Locate platelets.
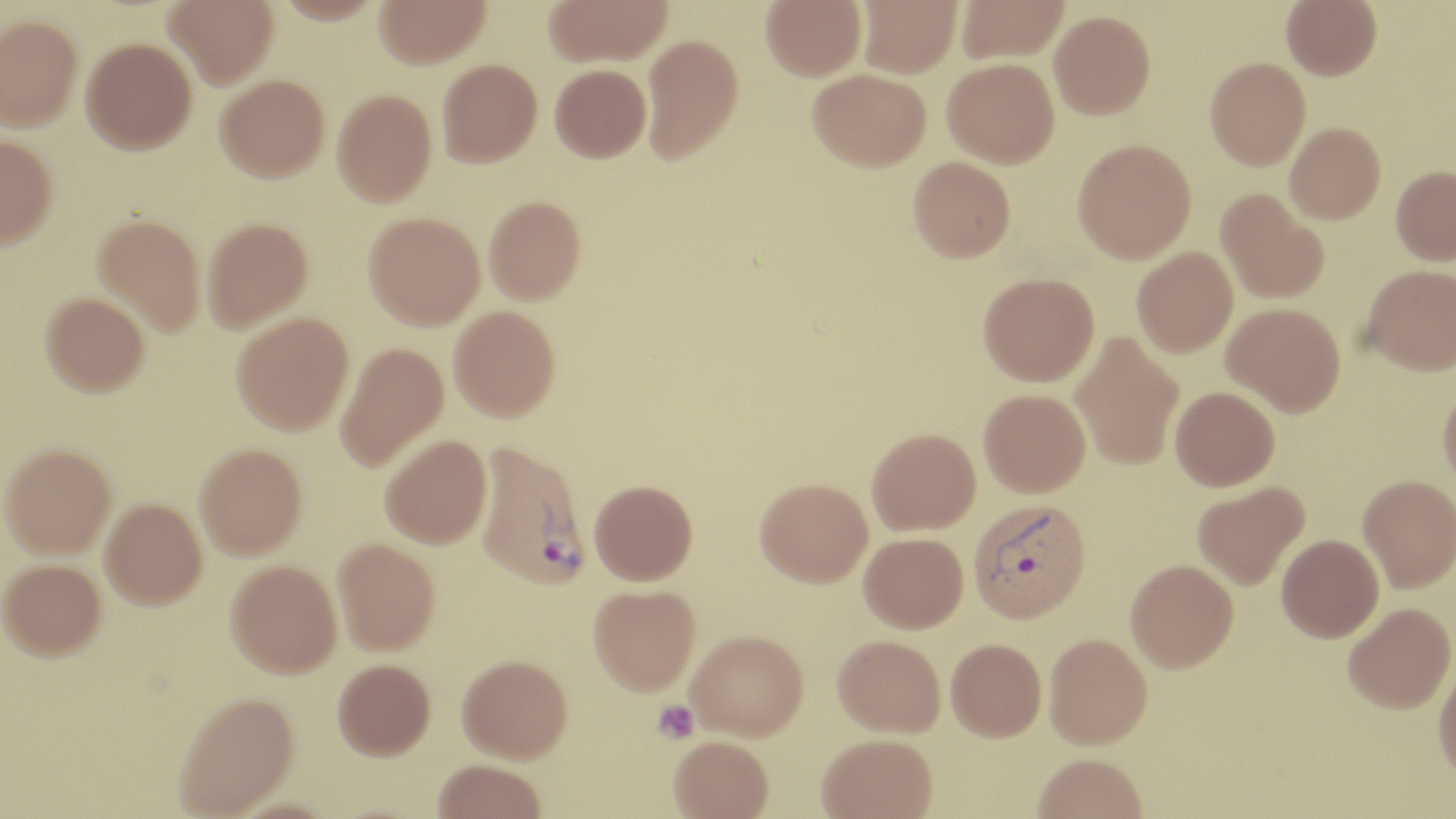

Approximate bounding boxes as (x1,y1)-(x2,y2) corner pairs in pixels.
Platelets: (653,700)-(700,744).

slide_level_diagnosis: Plasmodium vivax
uninfected_red_blood_cell_locations: 'approximate bounding boxes as (x1,y1)-(x2,y2) corner pairs in pixels: (164,0)-(278,88), (374,0)-(490,67), (543,0)-(673,66), (760,0)-(866,81), (857,0)-(962,77), (955,0)-(1070,63), (1281,0)-(1381,80), (1049,10)-(1155,119), (0,14)-(82,130), (641,34)-(744,164), (81,37)-(197,154), (1205,56)-(1310,170), (942,57)-(1060,167), (437,58)-(542,167), (549,64)-(651,162), (807,68)-(931,172), (215,74)-(330,182), (332,89)-(436,207), (1284,122)-(1386,224), (0,135)-(57,251), (1072,138)-(1196,263), (908,156)-(1016,262), (1391,166)-(1456,264), (1215,189)-(1329,304), (483,195)-(586,303), (363,212)-(485,329), (92,213)-(205,335), (202,217)-(313,332), (1132,247)-(1237,357), (1361,264)-(1456,375), (978,271)-(1099,386), (41,292)-(149,396), (1222,303)-(1345,415), (448,305)-(561,421), (231,312)-(353,435), (1069,330)-(1184,471), (334,342)-(449,472), (1437,383)-(1456,493), (1170,386)-(1280,490), (979,388)-(1090,497), (866,428)-(981,535), (379,435)-(492,549), (0,443)-(116,557), (194,443)-(307,559), (1358,474)-(1456,592), (754,477)-(872,587), (589,479)-(698,585), (1192,481)-(1310,590), (100,498)-(207,608), (858,532)-(969,633), (1277,534)-(1384,642), (332,538)-(440,655), (0,559)-(106,659), (225,559)-(342,678), (1125,559)-(1239,672), (588,584)-(700,696), (1342,602)-(1455,714), (686,629)-(808,740), (1044,632)-(1153,750), (833,635)-(946,738), (945,639)-(1046,742), (456,655)-(572,763), (1433,657)-(1456,787), (332,658)-(435,759), (172,690)-(300,818), (817,733)-(938,819), (669,736)-(773,819), (1031,755)-(1147,819), (433,760)-(547,819)'
stain: May-Grünwald-Giemsa
magnification: 1000x
field_of_view: single
plasmodium_vivax_infected_red_blood_cell_locations: 'approximate bounding boxes as (x1,y1)-(x2,y2) corner pairs in pixels: (474,439)-(589,590), (968,498)-(1091,624)'
preparation: thin blood smear
image_size: 1456×819 pixels
modality: light microscopy